Locate every blood parasite and identify its species.
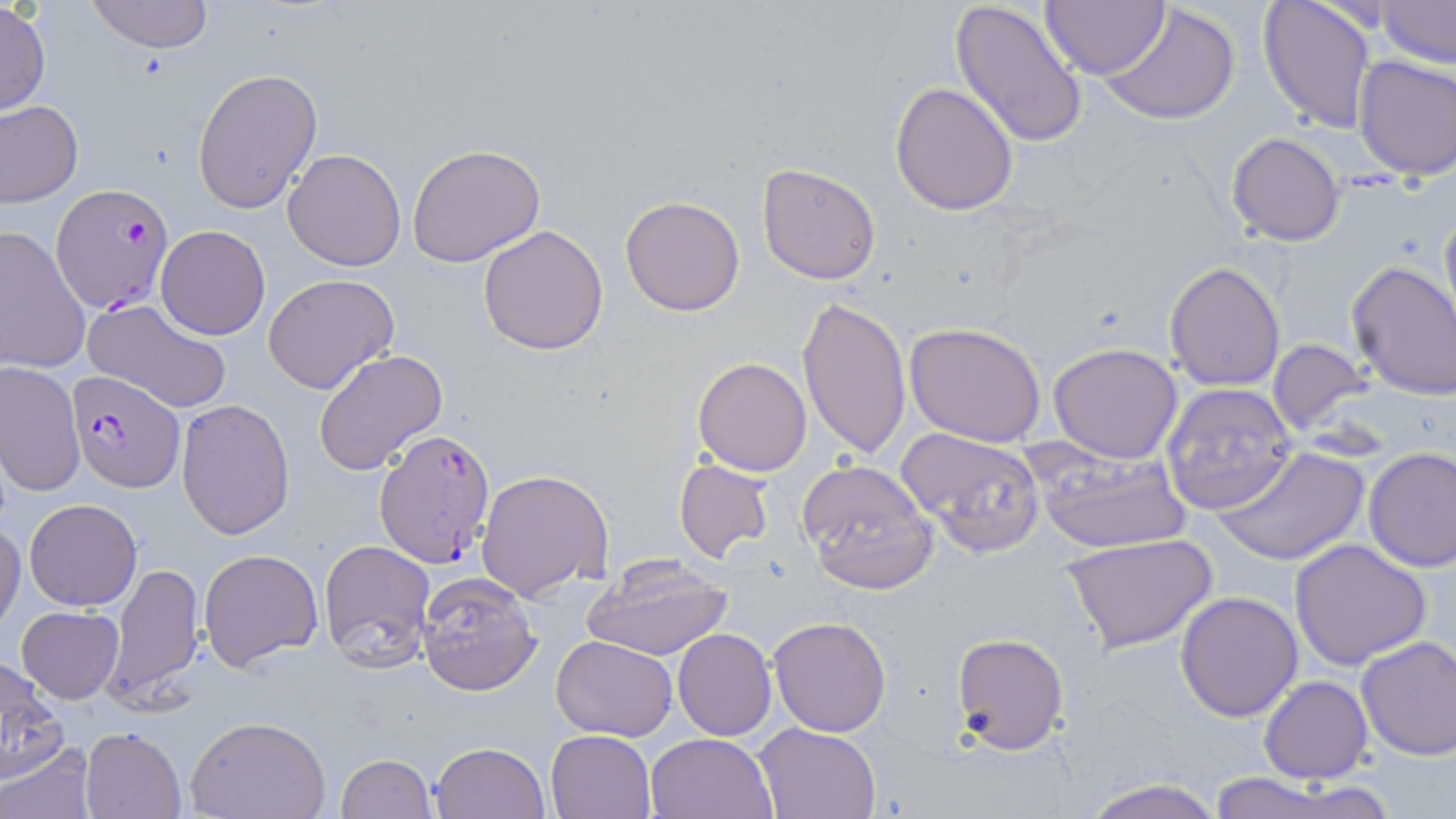

Approximate bounding boxes as [x1, y1, x2, y2] in pixels.
Plasmodium falciparum-infected red blood cells: [52, 183, 176, 314], [65, 372, 184, 491], [374, 427, 497, 570].
No Plasmodium ovale, Plasmodium malariae, Plasmodium vivax, Babesia divergens, or Trypanosoma brucei observed.

{
  "slide_level_diagnosis": "Plasmodium falciparum",
  "image_size": "1456×819 pixels",
  "uninfected_red_blood_cell_locations": "approximate bounding boxes as [x1, y1, x2, y2] in pixels: [950, 0, 1091, 147], [1042, 0, 1165, 80], [1259, 0, 1376, 133], [1375, 0, 1456, 68], [0, 1, 49, 119], [86, 1, 213, 53], [1101, 2, 1242, 127], [1354, 54, 1456, 180], [192, 66, 323, 213], [890, 81, 1019, 215], [1, 102, 82, 206], [1225, 132, 1345, 246], [407, 143, 547, 267], [283, 148, 406, 272], [757, 162, 883, 284], [619, 195, 746, 316], [1438, 205, 1456, 332], [156, 225, 271, 340], [478, 225, 609, 355], [0, 226, 93, 377], [1165, 261, 1286, 392], [1346, 261, 1456, 401], [263, 273, 400, 394], [797, 294, 911, 459], [84, 298, 232, 414], [904, 321, 1047, 446], [1268, 338, 1372, 436], [1047, 343, 1184, 463], [313, 348, 447, 475], [693, 356, 812, 475], [2, 361, 85, 497], [1160, 383, 1298, 516], [176, 399, 294, 541], [896, 426, 1048, 557], [1213, 446, 1369, 567], [1363, 447, 1456, 571], [1036, 449, 1192, 553], [673, 458, 775, 564], [797, 459, 937, 595], [477, 468, 614, 601], [24, 499, 142, 610], [0, 522, 25, 631], [1060, 534, 1218, 653], [319, 539, 436, 669], [1290, 539, 1431, 670], [199, 548, 324, 670], [582, 559, 734, 660], [106, 562, 203, 706], [416, 573, 542, 696], [1174, 592, 1304, 721], [16, 607, 123, 703], [769, 616, 892, 737], [673, 629, 776, 740], [951, 631, 1069, 754], [550, 635, 677, 740], [1355, 636, 1456, 761], [1, 659, 67, 781], [1260, 677, 1373, 784], [185, 716, 330, 819], [754, 722, 882, 818], [81, 727, 186, 818], [546, 728, 655, 818], [646, 732, 776, 818], [430, 741, 549, 819], [2, 742, 97, 819], [336, 754, 436, 819], [1200, 772, 1354, 819], [1078, 777, 1224, 819]",
  "field_of_view": "single",
  "stain": "May-Grünwald-Giemsa",
  "magnification": "1000x",
  "preparation": "thin blood smear",
  "modality": "optical microscopy"
}